Point out each malaria parasite.
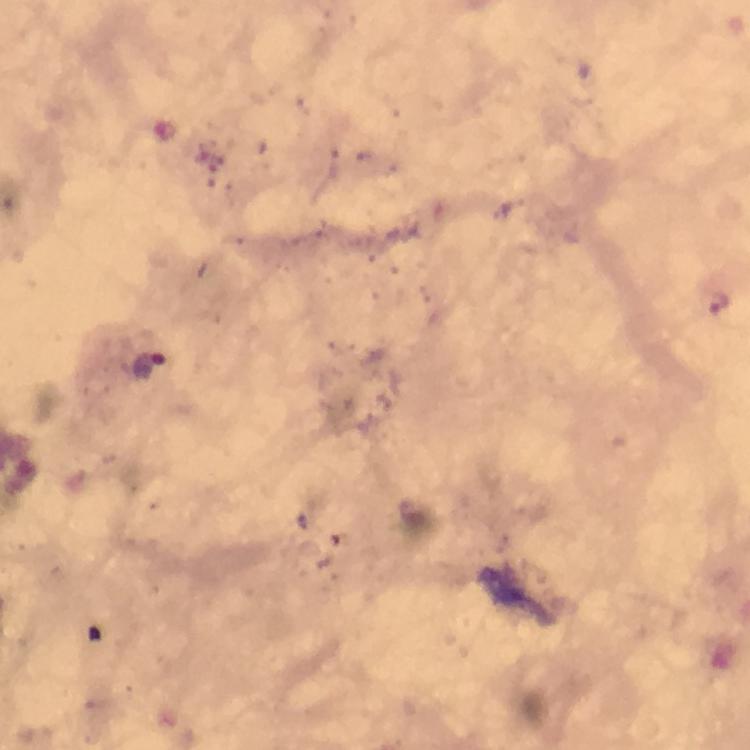
Approximate centers as [x, y] in pixels.
Malaria parasites: [718, 302], [148, 372].

Thick blood film. From a diagnostic examination for malaria. 100x magnification. Photographed through the microscope with a smartphone camera. Giemsa stain. Immersion oil applied. Image is 750×750 pixels. Cropped region of a single field of view.